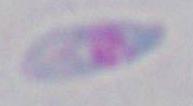

Summary:
  - Magnification: 1000x
  - Modality: micrograph
  - Identification: Toxoplasma gondii